Point out each Plasmodium parasite.
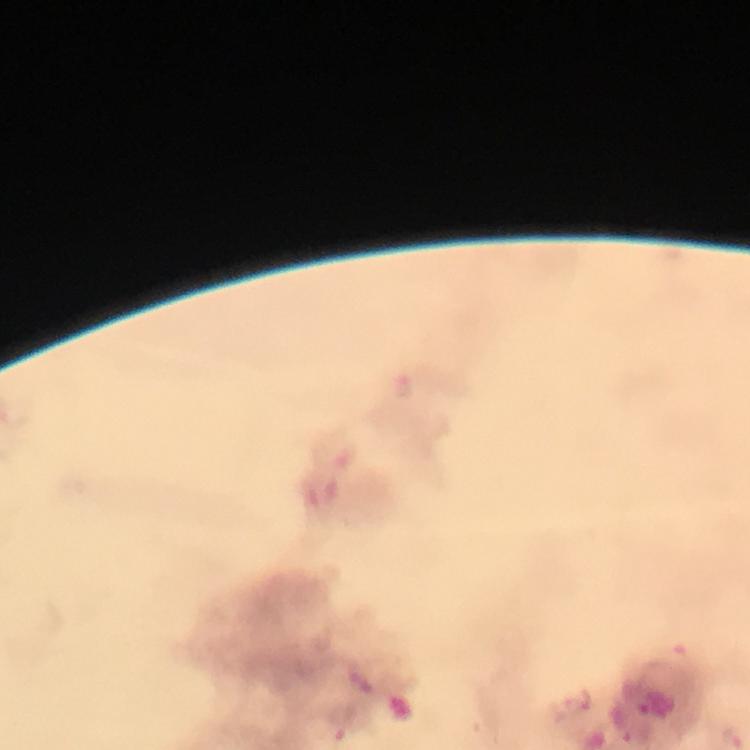

Approximate centers as {x, y} in pixels.
Plasmodium parasites: {579, 700}.

Summary:
  - Stain: Giemsa
  - Capture: smartphone camera through the microscope
  - Image size: 750×750 pixels
  - Magnification: 100x
  - Immersion oil: applied
  - Cropped from: a single field of view
  - Context: from a malaria diagnostic workup
  - Preparation: thick blood film